Assess the morphology of the red blood cells.
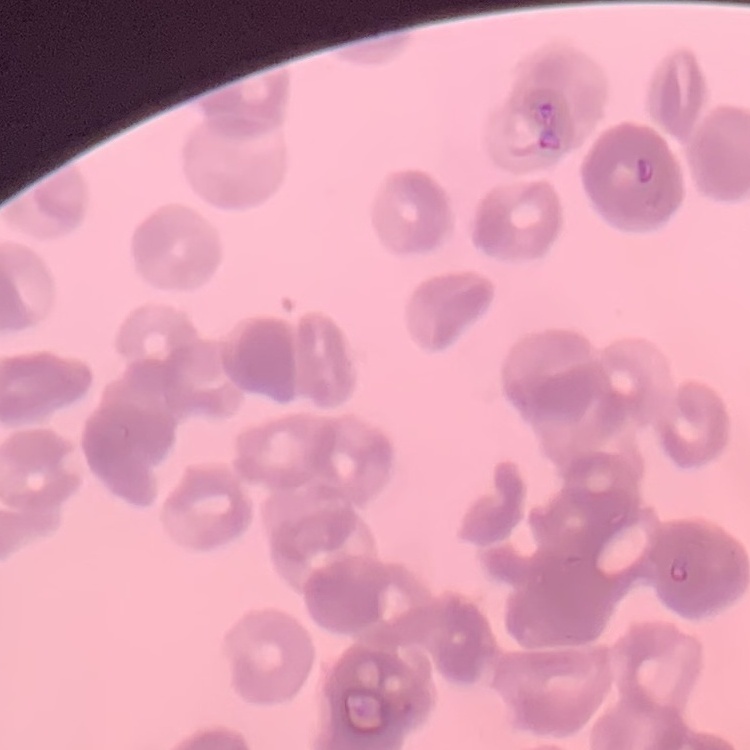
They show rouleaux formation.

Summary:
  - Image type: one tile cut from a larger photomicrograph
  - Stain: Field's or Giemsa
  - Preparation: thin blood film